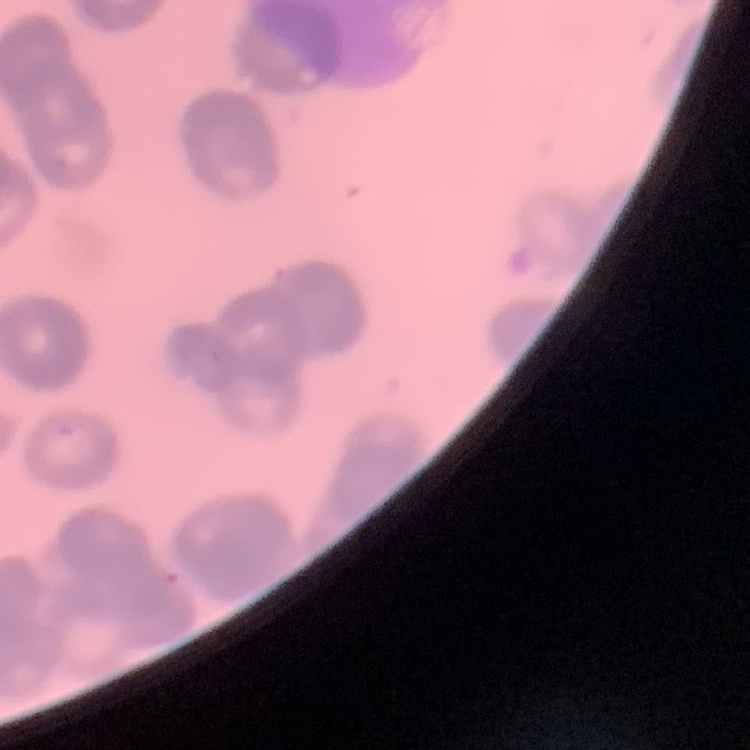

The red blood cells show rouleaux formation. Square crop of a larger photomicrograph. Field's or Giemsa stain. Thin blood film.